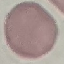
result: negative for malaria parasites
image_type: automatically extracted cell patch, resized to 64 × 64 pixels
capture: smartphone camera at the microscope eyepiece
stain: Giemsa
preparation: thin blood film